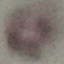
Summary:
  - Result: no malaria parasites detected
  - Stain: Giemsa
  - Preparation: thin blood smear
  - Capture: smartphone through the microscope eyepiece
  - Image type: automatically extracted cell patch, resized to 64 × 64 pixels